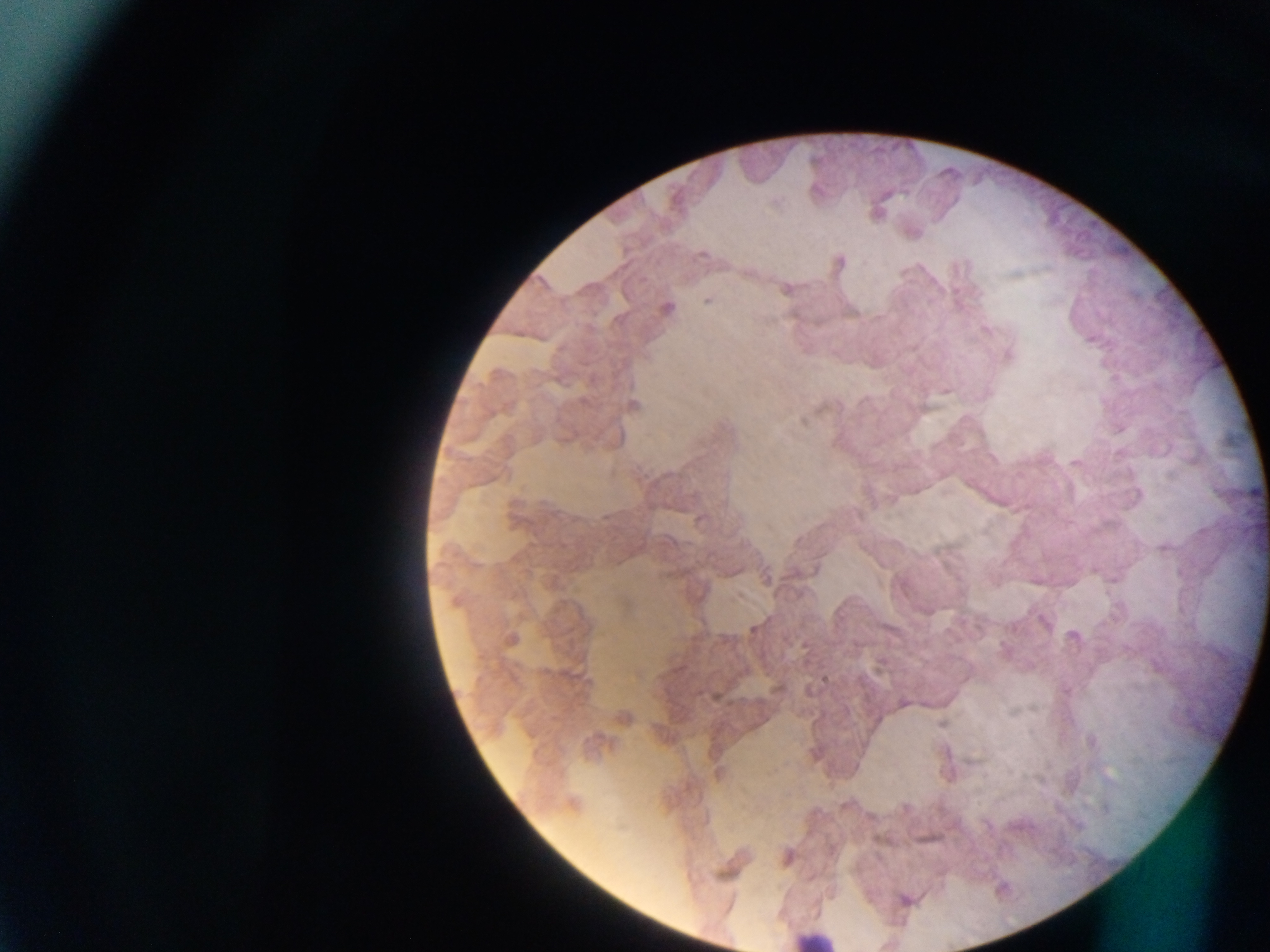

Approximate centers as x y in pixels.
Summary:
  - Leukocyte locations: 811 938
  - Malaria parasite locations: 910 231; 837 262; 786 289; 707 300; 665 308; 985 329; 1007 356; 945 390; 632 405; 1076 463; 699 519; 766 577; 1045 623; 1073 636; 511 640; 825 677; 903 703; 623 717; 719 774; 572 805; 786 857; 904 900
  - Preparation: thick blood film
  - Field of view: single
  - Capture: mobile-phone photograph through a microscope
  - Country: Ghana
  - Image size: 1270×952 pixels